Locate and identify every blood parasite.
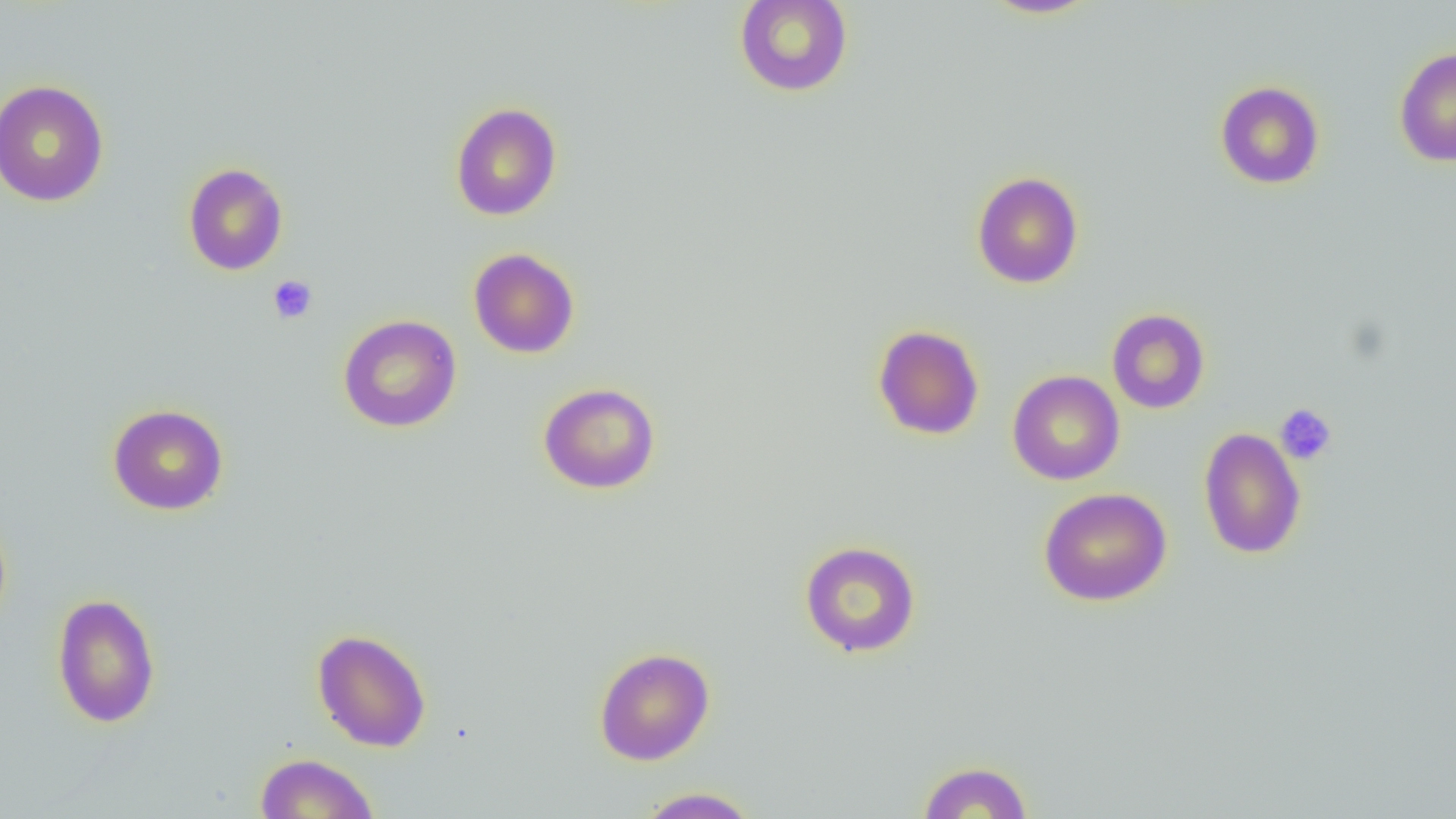

No blood parasites seen.

slide-level diagnosis = no evidence of blood parasites
platelet locations = approximate bounding boxes as (x1,y1)-(x2,y2) corner pairs in pixels: (268,275)-(317,324), (1275,403)-(1337,465)
uninfected red blood cell locations = approximate bounding boxes as (x1,y1)-(x2,y2) corner pairs in pixels: (734,0)-(853,97), (980,0)-(1101,19), (1394,46)-(1456,167), (0,79)-(110,207), (1215,80)-(1325,189), (450,102)-(562,221), (183,162)-(288,275), (971,171)-(1084,288), (468,248)-(580,359), (1107,308)-(1211,414), (337,314)-(462,433), (872,324)-(985,440), (1007,370)-(1124,485), (538,382)-(661,494), (107,403)-(230,516), (1198,427)-(1307,559), (1038,487)-(1173,607), (799,540)-(922,657), (51,592)-(161,729), (312,628)-(432,752), (593,647)-(715,766), (254,752)-(380,818), (917,759)-(1034,818), (635,787)-(760,818)
magnification = 1000x
field of view = single
modality = optical microscopy
image size = 1456×819 pixels
preparation = thin blood film